Locate every Plasmodium ovale-infected red blood cell.
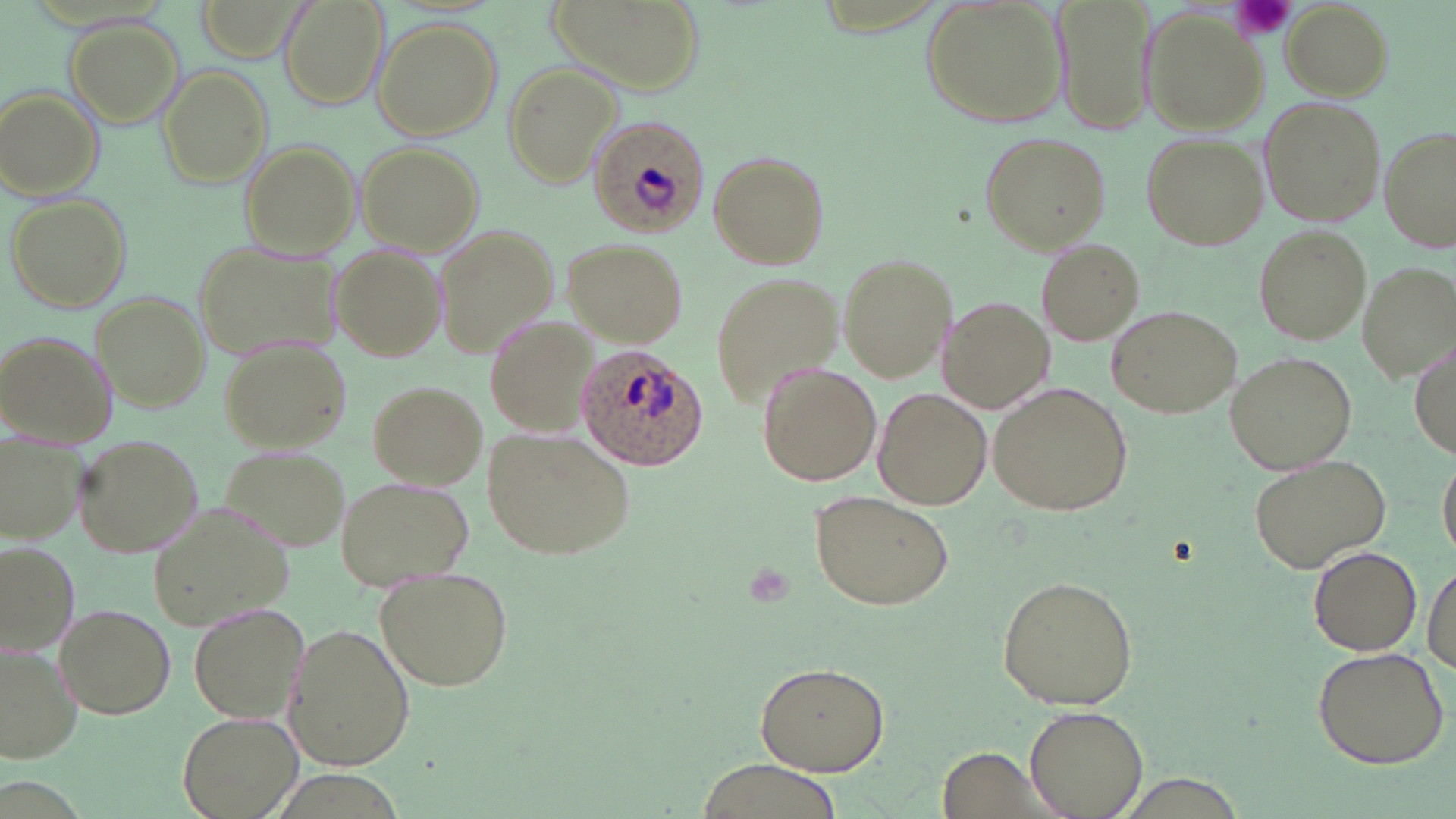

Approximate bounding boxes as named x1/y1/x2/y2 corners in pixels.
Plasmodium ovale-infected red blood cells: (x1=585, y1=113, x2=709, y2=240), (x1=577, y1=347, x2=707, y2=470).

Uninfected red blood cell locations: (x1=192, y1=0, x2=307, y2=62), (x1=278, y1=0, x2=388, y2=109), (x1=547, y1=0, x2=703, y2=98), (x1=1057, y1=0, x2=1153, y2=135), (x1=921, y1=1, x2=1070, y2=129), (x1=1282, y1=3, x2=1391, y2=99), (x1=1141, y1=13, x2=1265, y2=131), (x1=65, y1=17, x2=184, y2=128), (x1=371, y1=18, x2=504, y2=141), (x1=503, y1=63, x2=620, y2=189), (x1=156, y1=65, x2=273, y2=188), (x1=2, y1=87, x2=103, y2=198), (x1=1258, y1=98, x2=1385, y2=227), (x1=1381, y1=129, x2=1456, y2=253), (x1=979, y1=131, x2=1110, y2=255), (x1=1141, y1=133, x2=1269, y2=249), (x1=241, y1=141, x2=360, y2=257), (x1=357, y1=142, x2=486, y2=256), (x1=707, y1=151, x2=829, y2=269), (x1=6, y1=192, x2=132, y2=314), (x1=437, y1=224, x2=561, y2=359), (x1=1253, y1=224, x2=1372, y2=346), (x1=565, y1=237, x2=687, y2=348), (x1=1037, y1=238, x2=1144, y2=346), (x1=194, y1=239, x2=343, y2=358), (x1=331, y1=244, x2=445, y2=359), (x1=837, y1=253, x2=957, y2=385), (x1=1357, y1=261, x2=1454, y2=379), (x1=711, y1=274, x2=841, y2=406), (x1=95, y1=292, x2=209, y2=411), (x1=941, y1=298, x2=1052, y2=412), (x1=1105, y1=305, x2=1241, y2=420), (x1=485, y1=315, x2=596, y2=437), (x1=0, y1=330, x2=114, y2=446), (x1=1412, y1=335, x2=1455, y2=461), (x1=217, y1=336, x2=352, y2=451), (x1=1224, y1=350, x2=1358, y2=476), (x1=756, y1=361, x2=881, y2=486), (x1=369, y1=380, x2=488, y2=489), (x1=989, y1=380, x2=1134, y2=517), (x1=873, y1=387, x2=992, y2=510), (x1=482, y1=428, x2=633, y2=560), (x1=1, y1=431, x2=84, y2=548), (x1=72, y1=433, x2=205, y2=557), (x1=217, y1=444, x2=350, y2=552), (x1=1438, y1=450, x2=1456, y2=564), (x1=1249, y1=452, x2=1392, y2=574), (x1=336, y1=475, x2=476, y2=588), (x1=812, y1=489, x2=956, y2=609), (x1=149, y1=499, x2=299, y2=628), (x1=2, y1=543, x2=76, y2=657), (x1=1307, y1=543, x2=1422, y2=656), (x1=1425, y1=558, x2=1456, y2=675), (x1=376, y1=568, x2=516, y2=690), (x1=996, y1=577, x2=1139, y2=709), (x1=55, y1=603, x2=176, y2=719), (x1=190, y1=603, x2=309, y2=723), (x1=284, y1=624, x2=415, y2=771), (x1=1309, y1=645, x2=1451, y2=770), (x1=0, y1=646, x2=81, y2=765), (x1=756, y1=660, x2=890, y2=775), (x1=1026, y1=705, x2=1146, y2=819), (x1=176, y1=709, x2=303, y2=817), (x1=941, y1=746, x2=1049, y2=817), (x1=696, y1=760, x2=844, y2=819). Platelet locations: (x1=1227, y1=0, x2=1300, y2=43). Slide-level diagnosis: Plasmodium ovale. Thin blood film. Image is 1456×819 pixels. One field of a larger specimen. Captured at 1000x magnification. May-Grünwald-Giemsa-stained preparation. Optical microscopy.